Assess this cell for malaria.
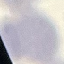

It is uninfected.

Summary:
  - Stain: Giemsa
  - Capture: smartphone through the microscope eyepiece
  - Image type: automatically extracted cell patch, resized to 64 × 64 pixels
  - Preparation: thin smear